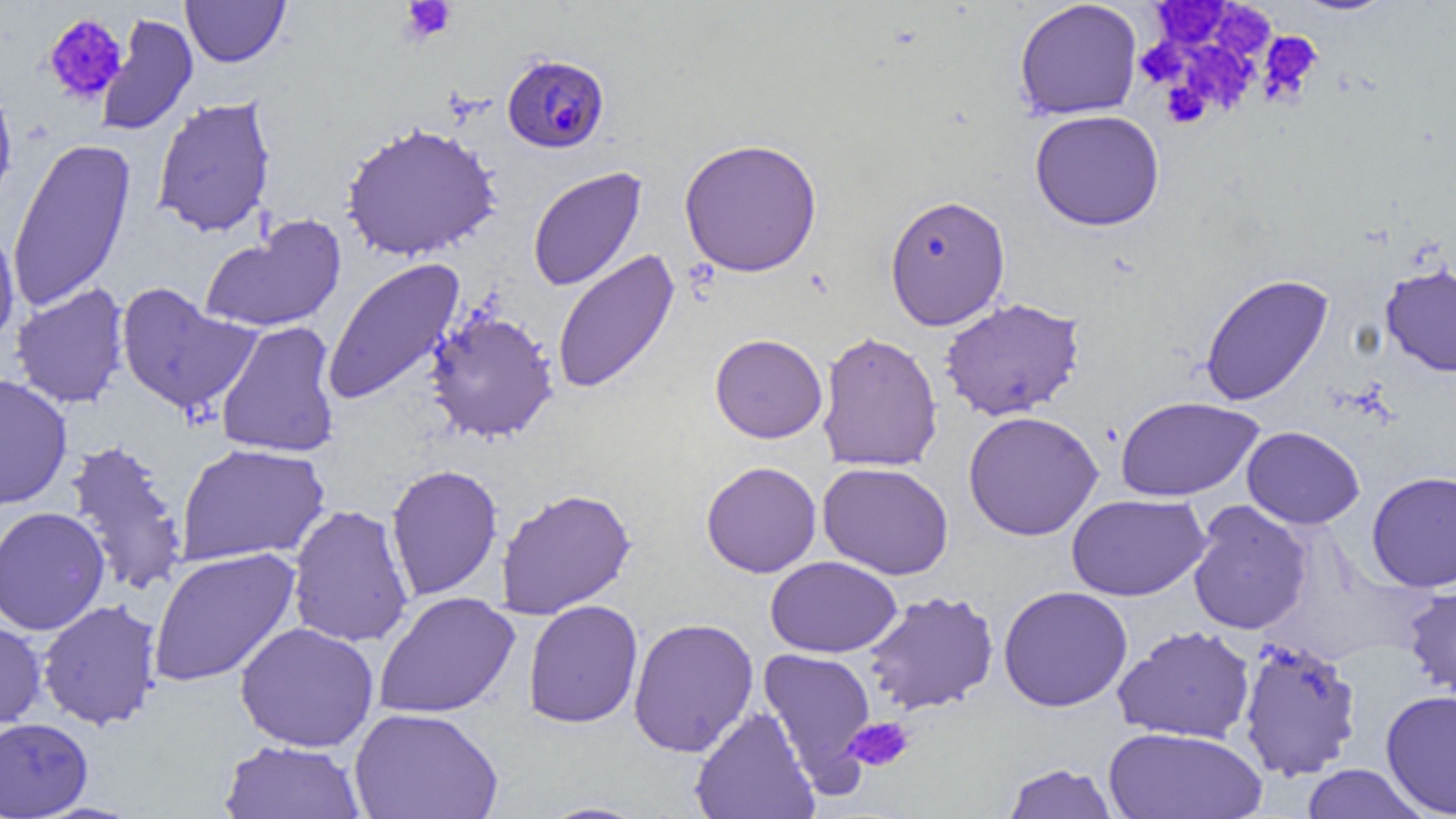

slide_level_diagnosis: Plasmodium falciparum
preparation: thin blood smear
plasmodium_falciparum_infected_red_blood_cell_locations: 'approximate bounding boxes as [x1, y1, x2, y2] in pixels: [502, 53, 610, 154]'
uninfected_red_blood_cell_locations: 'approximate bounding boxes as [x1, y1, x2, y2] in pixels: [181, 0, 290, 68], [1290, 0, 1399, 16], [1014, 1, 1143, 120], [95, 14, 198, 136], [0, 80, 18, 211], [151, 96, 277, 238], [1030, 109, 1165, 231], [340, 121, 503, 262], [8, 137, 137, 313], [678, 137, 823, 277], [528, 166, 647, 292], [884, 194, 1011, 331], [198, 214, 349, 335], [0, 221, 21, 349], [552, 249, 681, 395], [322, 257, 466, 406], [1380, 264, 1456, 376], [1200, 273, 1334, 406], [10, 282, 130, 409], [114, 282, 261, 418], [939, 297, 1085, 421], [424, 309, 559, 443], [215, 321, 341, 458], [816, 330, 943, 473], [710, 333, 827, 443], [0, 374, 72, 510], [1114, 396, 1264, 501], [963, 410, 1103, 541], [1242, 425, 1365, 529], [64, 438, 189, 597], [176, 443, 330, 567], [701, 461, 822, 578], [817, 462, 954, 580], [385, 464, 503, 601], [1366, 470, 1456, 592], [496, 488, 636, 619], [1066, 493, 1210, 601], [1186, 500, 1312, 635], [286, 503, 414, 648], [0, 506, 110, 635], [148, 547, 301, 687], [765, 555, 902, 658], [1403, 584, 1456, 699], [998, 585, 1133, 712], [862, 590, 999, 715], [373, 591, 520, 719], [37, 599, 162, 730], [523, 599, 643, 729], [0, 617, 47, 731], [628, 617, 759, 757], [235, 622, 380, 753], [1113, 624, 1256, 744], [1238, 635, 1364, 780], [758, 647, 877, 781], [1380, 690, 1456, 817], [690, 706, 819, 819], [349, 707, 504, 819], [0, 717, 93, 819], [1104, 726, 1268, 818], [219, 739, 366, 818], [1001, 762, 1121, 819], [1299, 764, 1433, 819], [534, 801, 653, 819]'
image_size: 1456×819 pixels
modality: light microscopy
platelet_locations: 'approximate bounding boxes as [x1, y1, x2, y2] in pixels: [398, 1, 458, 45], [1154, 2, 1231, 48], [1219, 9, 1278, 62], [43, 13, 128, 105], [1258, 31, 1321, 103], [1136, 40, 1187, 87], [1184, 43, 1258, 113], [1162, 81, 1210, 129], [844, 715, 915, 772]'
magnification: 1000x
field_of_view: one of a larger specimen